Report the malaria status of this cell.
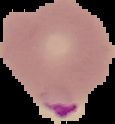
Parasitized.

image type = segmented cell region on a black background
image size = 115×124 pixels
preparation = thin blood film